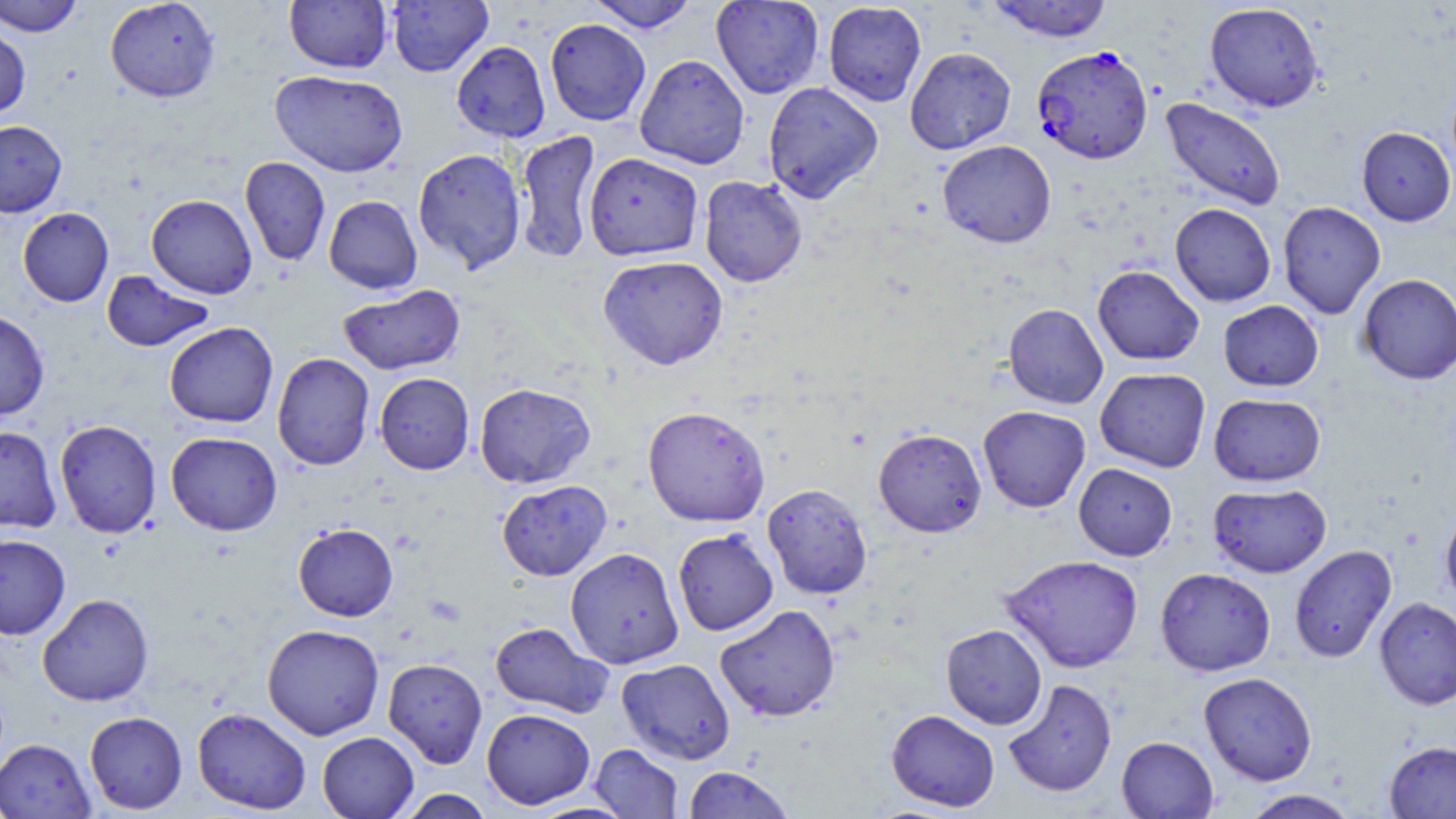
Summary:
  - Coordinate format: approximate bounding boxes as [x1, y1, x2, y2] in pixels
  - Uninfected red blood cell locations: [0, 0, 84, 37], [104, 0, 221, 103], [285, 0, 392, 74], [386, 0, 493, 77], [585, 0, 701, 32], [711, 0, 824, 99], [986, 0, 1114, 42], [823, 1, 927, 107], [1204, 2, 1325, 113], [544, 18, 651, 126], [0, 23, 31, 120], [451, 41, 551, 142], [905, 46, 1016, 154], [634, 54, 750, 169], [270, 70, 408, 177], [762, 82, 884, 203], [1160, 97, 1287, 211], [0, 120, 67, 217], [1356, 126, 1455, 226], [515, 129, 601, 265], [937, 140, 1057, 248], [413, 148, 527, 274], [584, 152, 703, 261], [239, 156, 330, 266], [698, 175, 808, 288], [146, 194, 258, 299], [323, 195, 423, 294], [1277, 201, 1386, 319], [1170, 203, 1276, 307], [17, 207, 114, 307], [598, 255, 729, 370], [1092, 265, 1204, 366], [101, 270, 215, 353], [1357, 273, 1456, 384], [338, 284, 466, 375], [1218, 300, 1324, 392], [1003, 303, 1109, 409], [0, 310, 50, 420], [164, 322, 279, 428], [272, 352, 375, 471], [1095, 368, 1211, 472], [374, 372, 475, 475], [474, 382, 595, 489], [1208, 393, 1326, 486], [642, 405, 771, 527], [978, 405, 1091, 513], [54, 419, 162, 538], [0, 426, 62, 533], [873, 428, 987, 537], [166, 431, 282, 536], [1073, 463, 1177, 561], [496, 480, 612, 581], [762, 483, 873, 600], [1207, 483, 1332, 578], [1440, 504, 1456, 609], [293, 523, 398, 621], [672, 528, 779, 636], [0, 534, 70, 639], [1289, 544, 1397, 663], [565, 547, 684, 669], [1000, 554, 1144, 673], [1155, 567, 1276, 676], [37, 593, 154, 706], [1374, 597, 1456, 710], [715, 604, 841, 722], [489, 621, 613, 718], [262, 624, 385, 740], [940, 624, 1048, 730], [383, 658, 488, 768], [617, 658, 735, 765], [1198, 672, 1318, 786], [1002, 678, 1117, 798], [192, 707, 311, 814], [482, 708, 595, 809], [886, 709, 1000, 812], [84, 711, 188, 814], [317, 731, 419, 818], [1116, 735, 1218, 818], [0, 738, 95, 819], [1384, 741, 1456, 818], [590, 743, 684, 818], [682, 765, 797, 819], [396, 789, 494, 819], [1240, 789, 1361, 819]
  - Plasmodium falciparum-infected red blood cell locations: [1031, 45, 1153, 165]
  - Slide-level diagnosis: Plasmodium falciparum
  - Modality: light microscopy
  - Magnification: 1000x
  - Stain: May-Grünwald-Giemsa
  - Image size: 1456×819 pixels
  - Field of view: one of a larger specimen
  - Preparation: thin blood smear